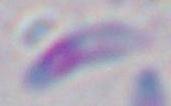
Summary:
  - Modality: micrograph
  - Magnification: 1000x
  - Identification: Toxoplasma gondii